State the preparation type.
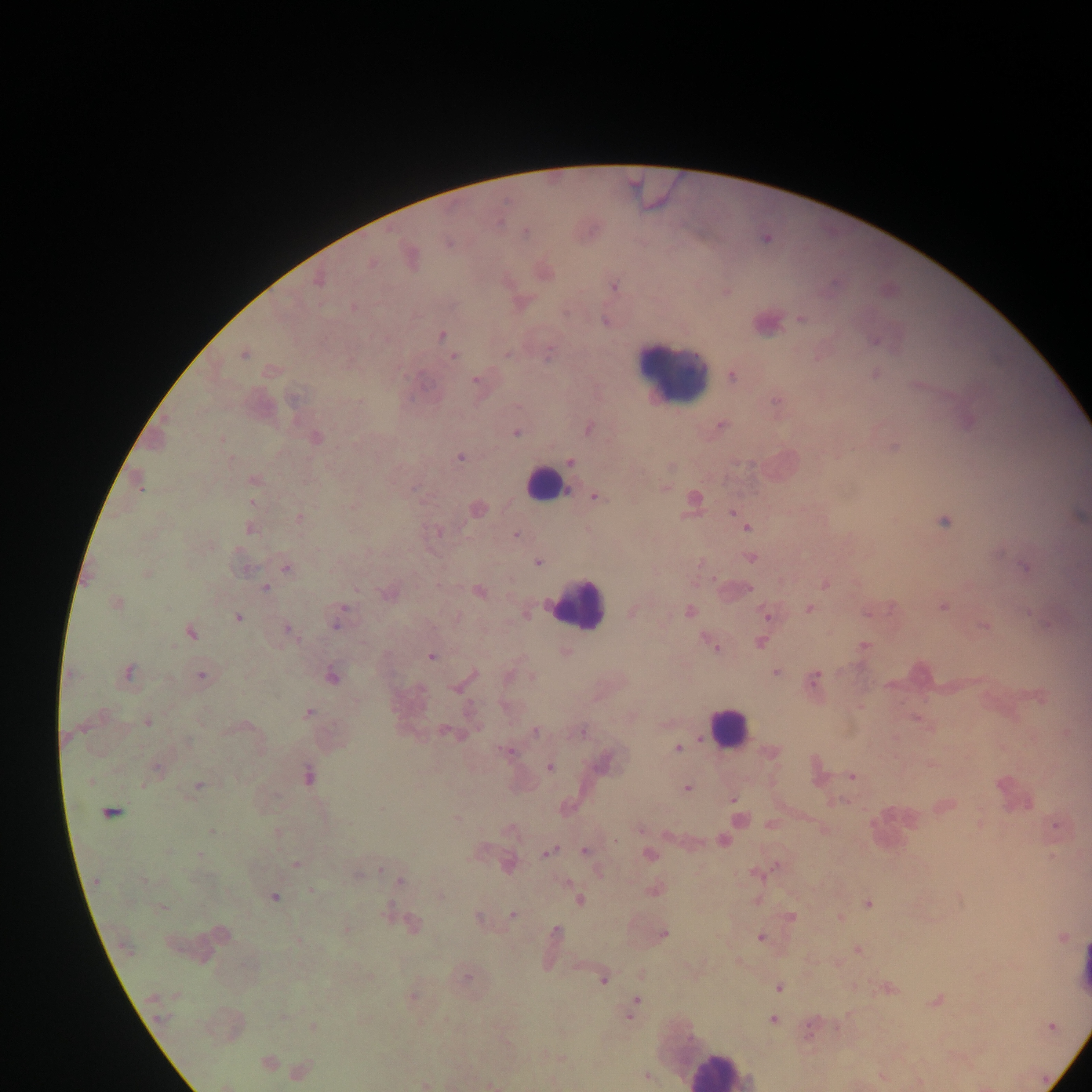
Thick blood smear.

Approximate centers as x y in pixels. Plasmodium parasite locations: 525 231; 765 238; 448 242; 409 255; 370 263; 543 271; 317 279; 613 286; 726 291; 352 307; 800 318; 606 320; 765 322; 441 334; 875 340; 244 353; 548 353; 454 357; 271 370; 875 374; 731 375; 475 380; 776 402; 721 426; 588 427; 516 432; 314 438; 221 439; 894 447; 460 456; 570 461; 253 479; 139 482; 663 487; 595 496; 692 499; 252 502; 476 509; 732 512; 1077 515; 298 519; 944 521; 747 527; 250 528; 436 530; 516 535; 751 557; 537 561; 286 567; 1025 567; 146 574; 824 583; 264 587; 737 590; 478 591; 389 593; 116 603; 942 606; 809 608; 870 610; 632 611; 689 611; 1027 611; 525 612; 765 613; 237 617; 338 619; 1049 623; 984 624; 288 629; 189 631; 761 642; 713 643; 863 646; 564 651; 430 656; 127 672; 775 672; 201 675; 508 676; 332 677; 532 678; 813 679; 463 682; 1038 695; 308 712; 917 718; 147 720; 447 732; 534 732; 580 732; 1065 732; 677 747; 506 752; 771 753; 603 761; 930 764; 549 767; 156 769; 816 771; 307 775; 852 776; 198 786; 686 788; 732 800; 839 800; 944 805; 109 813; 457 818; 739 820; 980 823; 770 824; 1056 824; 640 828; 212 832; 276 833; 723 840; 585 851; 548 852; 649 854; 199 855; 295 863; 507 864; 776 864; 379 870; 598 871; 756 873; 399 881; 653 889; 312 891; 273 896; 439 896; 578 900; 757 900; 867 903; 162 907; 513 914; 791 917; 479 918; 840 918; 410 924; 345 931; 556 932; 220 933; 662 934; 760 937; 1061 937; 298 939; 857 949; 465 976; 604 977; 779 986; 887 988; 411 996; 936 1000; 634 1006; 773 1020; 313 1027; 1050 1027; 810 1028; 561 1058; 267 1062; 299 1072; 647 1076; 882 1076; 918 1082; 424 1084; 226 1085; 491 1085. Leukocyte locations: 673 369; 545 483; 574 603; 727 727; 893 828; 1082 971; 720 1070. One field of view. Image is 1092×1092 pixels. Collected in Ghana. Mobile-phone photograph taken through the microscope.